Assess this cell for malaria.
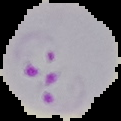
Parasitized.

Summary:
  - Preparation: thin blood smear
  - Image type: cell region segmented out of the field of view; surrounding area masked to black
  - Image size: 121×121 pixels